Identify the blood parasite species.
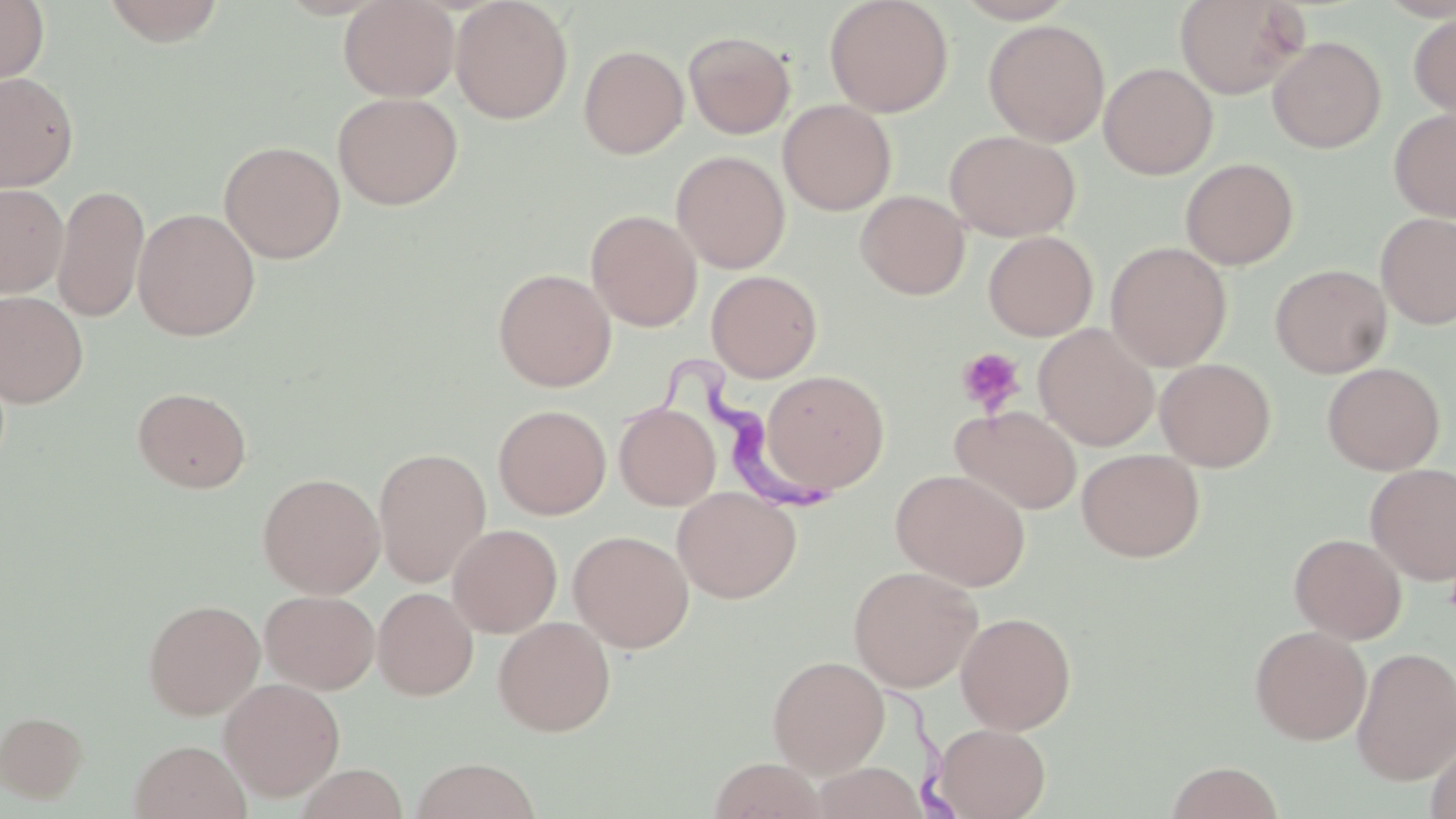
Trypanosoma brucei.

Summary:
  - Coordinate format: approximate bounding boxes as (x1,y1)-(x2,y2) corner pairs in pixels
  - Platelet locations: (955,347)-(1026,417)
  - Uninfected red blood cell locations: (0,0)-(49,89), (101,0)-(227,46), (338,0)-(459,101), (450,0)-(573,124), (824,0)-(954,117), (1175,0)-(1309,99), (1409,10)-(1456,121), (983,19)-(1110,146), (683,31)-(795,139), (1267,36)-(1386,153), (579,44)-(689,159), (1099,62)-(1218,179), (0,71)-(79,191), (332,92)-(464,210), (777,99)-(896,215), (1389,108)-(1456,222), (945,129)-(1081,241), (218,140)-(346,263), (671,150)-(790,273), (1180,158)-(1299,270), (0,182)-(69,298), (52,183)-(149,323), (856,190)-(970,299), (133,208)-(260,341), (586,209)-(702,331), (1376,212)-(1456,328), (983,230)-(1098,341), (1106,242)-(1232,371), (1270,263)-(1392,378), (493,268)-(616,391), (706,270)-(823,382), (0,290)-(89,408), (1034,324)-(1159,450), (1155,357)-(1276,471), (1322,362)-(1445,475), (760,370)-(890,493), (132,387)-(252,493), (614,402)-(720,510), (493,404)-(611,520), (951,405)-(1081,515), (373,446)-(492,587), (1076,448)-(1205,562), (1365,463)-(1456,584), (891,468)-(1030,591), (257,472)-(385,598), (673,486)-(801,603), (448,524)-(562,636), (568,530)-(694,653), (1289,532)-(1407,644), (848,564)-(982,692), (373,587)-(478,700), (259,589)-(380,694), (143,598)-(265,720), (956,611)-(1076,734), (493,616)-(616,736), (1249,625)-(1371,744), (1351,646)-(1456,786), (767,655)-(890,776), (219,677)-(345,801), (1,710)-(88,803), (933,723)-(1051,819), (1425,735)-(1456,819), (129,739)-(251,819), (409,757)-(542,819), (707,757)-(828,819), (1165,761)-(1285,819), (808,762)-(928,819), (294,764)-(409,819)
  - Trypanosoma brucei locations: (639,356)-(849,521), (889,688)-(957,818)
  - Field of view: one of a larger specimen
  - Image size: 1456×819 pixels
  - Magnification: 1000x
  - Modality: optical microscopy
  - Preparation: thin blood film
  - Stain: May-Grünwald-Giemsa